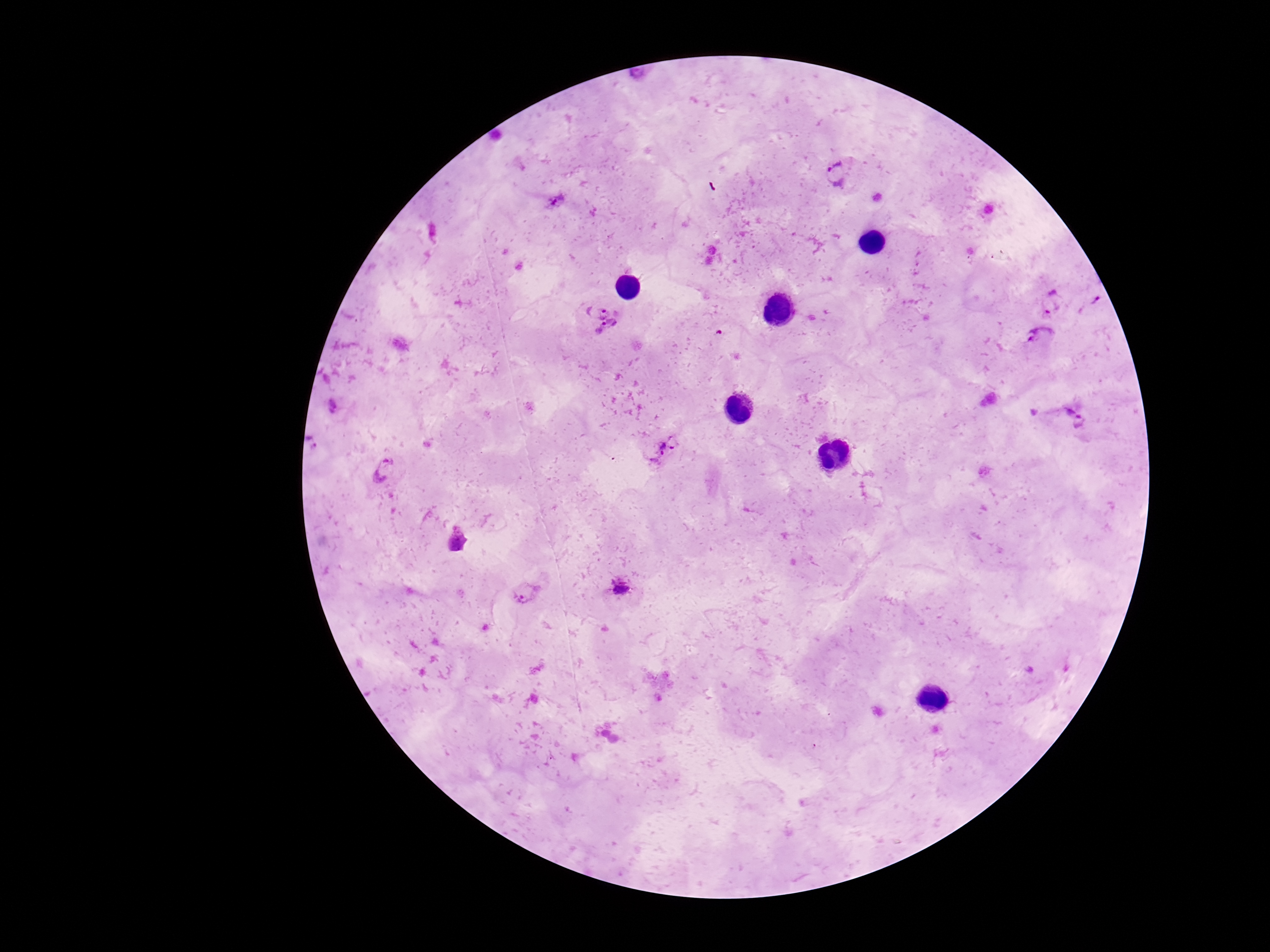

magnification = 100x
capture = smartphone camera through the microscope eyepiece
stain = Giemsa
field of view = one from this slide
image size = 1270×952 pixels
patient malaria status = positive
preparation = thick blood film
Plasmodium parasite locations = approximate centers as {x, y} in pixels: {841, 173}, {555, 200}, {1051, 301}, {1094, 305}, {596, 309}, {610, 333}, {1040, 340}, {1076, 416}, {665, 451}, {385, 469}, {458, 541}, {620, 586}, {525, 592}